Name the blood parasite species.
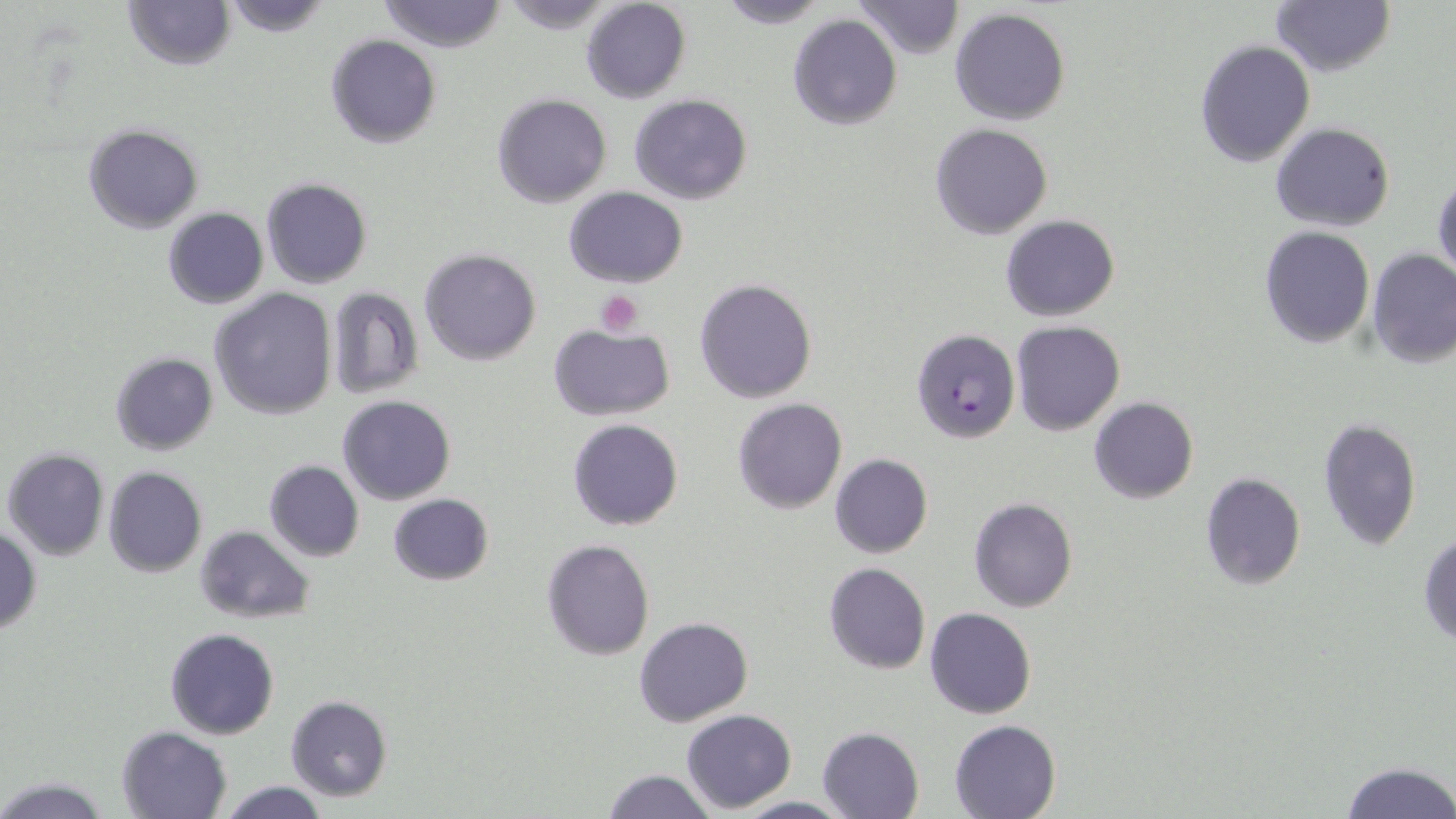
Plasmodium falciparum.

preparation: thin blood film
plasmodium_falciparum_infected_red_blood_cell_locations: 'approximate bounding boxes as [x1, y1, x2, y2] in pixels: [912, 328, 1020, 445]'
field_of_view: single
image_size: 1456×819 pixels
uninfected_red_blood_cell_locations: 'approximate bounding boxes as [x1, y1, x2, y2] in pixels: [121, 0, 235, 71], [222, 0, 333, 38], [377, 0, 507, 53], [496, 0, 624, 31], [714, 0, 830, 29], [854, 0, 965, 59], [580, 1, 690, 103], [1272, 1, 1394, 78], [950, 8, 1072, 126], [787, 13, 903, 130], [325, 34, 442, 150], [1194, 39, 1317, 170], [493, 94, 611, 207], [629, 95, 752, 205], [83, 123, 203, 233], [930, 123, 1053, 239], [1270, 123, 1395, 232], [1434, 173, 1455, 284], [260, 177, 373, 288], [563, 187, 688, 288], [162, 208, 267, 309], [1001, 214, 1120, 321], [1259, 227, 1374, 348], [1367, 247, 1456, 370], [419, 248, 541, 366], [695, 278, 817, 403], [326, 288, 424, 400], [209, 289, 337, 420], [1010, 321, 1125, 435], [548, 324, 674, 419], [109, 351, 219, 456], [337, 394, 456, 506], [1088, 397, 1198, 503], [732, 398, 847, 513], [1317, 417, 1422, 552], [568, 418, 684, 531], [3, 448, 109, 560], [829, 454, 932, 558], [264, 460, 364, 562], [102, 468, 207, 579], [1198, 472, 1307, 592], [387, 495, 493, 586], [969, 497, 1078, 612], [0, 525, 40, 634], [195, 525, 315, 625], [1419, 532, 1456, 647], [541, 538, 655, 660], [824, 563, 931, 674], [924, 607, 1037, 718], [633, 616, 754, 728], [165, 628, 278, 739], [285, 695, 391, 802], [682, 709, 796, 811], [949, 719, 1062, 819], [116, 725, 232, 818], [816, 726, 923, 819], [1336, 760, 1455, 819], [603, 770, 718, 818], [0, 776, 110, 817], [215, 780, 330, 818], [734, 796, 851, 817]'
stain: May-Grünwald-Giemsa
modality: optical microscopy
magnification: 1000x
platelet_locations: 'approximate bounding boxes as [x1, y1, x2, y2] in pixels: [595, 291, 643, 336]'